Comment on the morphology of the red blood cells.
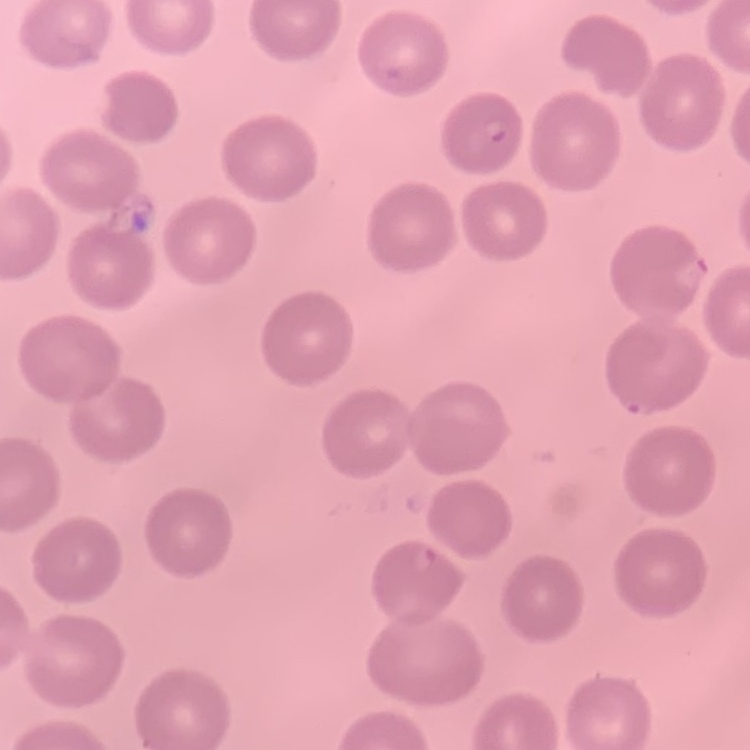

They show no rouleaux formation.

One tile cut from a larger photomicrograph. Thin blood film. Stained with either Field's or Giemsa.